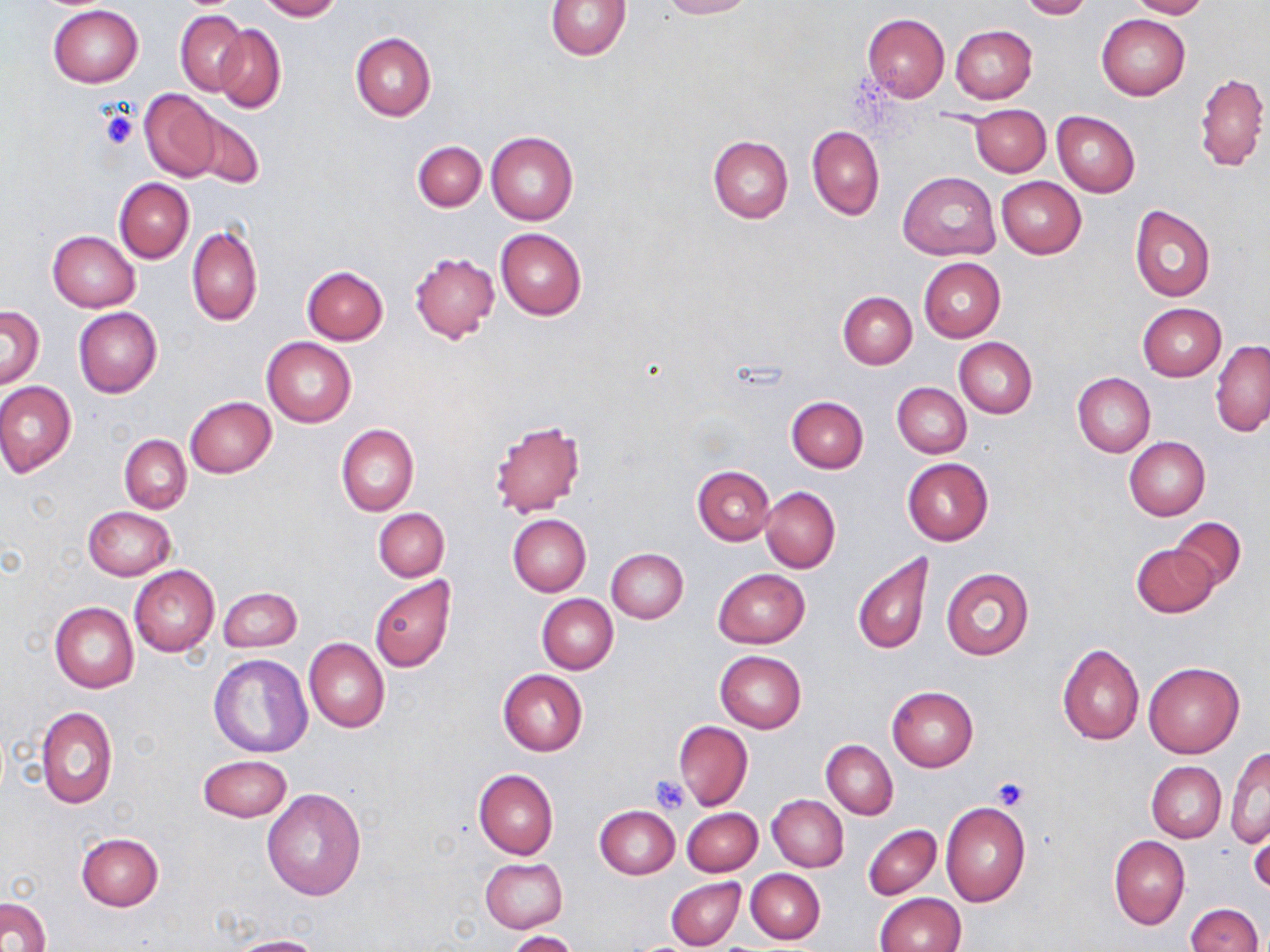

Approximate bounding boxes as named x1/y1/x2/y2 corners in pixels. Uninfected red blood cell locations: (x1=257, y1=0, x2=342, y2=21), (x1=546, y1=0, x2=632, y2=60), (x1=657, y1=0, x2=753, y2=19), (x1=1018, y1=0, x2=1092, y2=20), (x1=1126, y1=0, x2=1209, y2=18), (x1=49, y1=5, x2=142, y2=86), (x1=176, y1=11, x2=248, y2=95), (x1=861, y1=14, x2=950, y2=102), (x1=1097, y1=14, x2=1190, y2=100), (x1=214, y1=24, x2=286, y2=112), (x1=950, y1=25, x2=1037, y2=103), (x1=351, y1=31, x2=435, y2=120), (x1=1193, y1=72, x2=1268, y2=172), (x1=139, y1=89, x2=223, y2=181), (x1=971, y1=105, x2=1050, y2=175), (x1=1052, y1=111, x2=1140, y2=197), (x1=188, y1=112, x2=263, y2=190), (x1=808, y1=125, x2=884, y2=220), (x1=486, y1=131, x2=579, y2=225), (x1=708, y1=136, x2=793, y2=222), (x1=413, y1=140, x2=485, y2=212), (x1=898, y1=171, x2=998, y2=261), (x1=996, y1=176, x2=1087, y2=258), (x1=114, y1=178, x2=194, y2=262), (x1=1129, y1=205, x2=1216, y2=304), (x1=187, y1=225, x2=262, y2=326), (x1=496, y1=229, x2=587, y2=320), (x1=48, y1=230, x2=139, y2=311), (x1=409, y1=251, x2=499, y2=343), (x1=918, y1=258, x2=1005, y2=342), (x1=302, y1=267, x2=388, y2=345), (x1=838, y1=291, x2=917, y2=369), (x1=1137, y1=303, x2=1226, y2=381), (x1=0, y1=305, x2=44, y2=388), (x1=74, y1=306, x2=162, y2=399), (x1=261, y1=338, x2=356, y2=428), (x1=954, y1=338, x2=1037, y2=418), (x1=1210, y1=340, x2=1270, y2=437), (x1=1073, y1=372, x2=1154, y2=458), (x1=0, y1=381, x2=76, y2=478), (x1=892, y1=381, x2=971, y2=457), (x1=184, y1=396, x2=276, y2=478), (x1=787, y1=397, x2=868, y2=472), (x1=488, y1=420, x2=585, y2=519), (x1=336, y1=425, x2=417, y2=516), (x1=119, y1=434, x2=191, y2=513), (x1=1124, y1=437, x2=1210, y2=521), (x1=902, y1=458, x2=994, y2=546), (x1=693, y1=466, x2=774, y2=544), (x1=760, y1=486, x2=840, y2=573), (x1=85, y1=506, x2=175, y2=580), (x1=374, y1=508, x2=449, y2=581), (x1=508, y1=514, x2=591, y2=596), (x1=1171, y1=517, x2=1245, y2=590), (x1=1132, y1=543, x2=1218, y2=617), (x1=606, y1=547, x2=689, y2=623), (x1=852, y1=553, x2=933, y2=654), (x1=129, y1=565, x2=220, y2=657), (x1=940, y1=567, x2=1034, y2=661), (x1=713, y1=568, x2=809, y2=648), (x1=369, y1=577, x2=455, y2=673), (x1=218, y1=586, x2=301, y2=652), (x1=537, y1=594, x2=618, y2=674), (x1=49, y1=601, x2=139, y2=692), (x1=303, y1=638, x2=389, y2=733), (x1=1057, y1=643, x2=1145, y2=745), (x1=715, y1=651, x2=806, y2=732), (x1=208, y1=653, x2=314, y2=759), (x1=1143, y1=661, x2=1245, y2=759), (x1=498, y1=669, x2=587, y2=755), (x1=887, y1=686, x2=978, y2=771), (x1=36, y1=706, x2=117, y2=808), (x1=674, y1=720, x2=753, y2=810), (x1=823, y1=740, x2=897, y2=819), (x1=1226, y1=749, x2=1269, y2=849), (x1=198, y1=754, x2=292, y2=821), (x1=1146, y1=761, x2=1226, y2=843), (x1=474, y1=768, x2=558, y2=859), (x1=262, y1=787, x2=366, y2=900), (x1=767, y1=794, x2=848, y2=872), (x1=940, y1=801, x2=1032, y2=907), (x1=677, y1=805, x2=754, y2=946), (x1=595, y1=806, x2=679, y2=879), (x1=682, y1=808, x2=762, y2=876), (x1=1248, y1=820, x2=1269, y2=897), (x1=862, y1=824, x2=941, y2=900), (x1=76, y1=831, x2=163, y2=911), (x1=1109, y1=835, x2=1189, y2=930), (x1=480, y1=858, x2=568, y2=933), (x1=746, y1=869, x2=825, y2=944), (x1=666, y1=878, x2=743, y2=949), (x1=875, y1=892, x2=964, y2=952), (x1=2, y1=897, x2=51, y2=952), (x1=1186, y1=903, x2=1264, y2=952), (x1=507, y1=930, x2=579, y2=952), (x1=226, y1=935, x2=326, y2=952). Platelet locations: (x1=100, y1=108, x2=138, y2=149), (x1=649, y1=774, x2=690, y2=813), (x1=993, y1=777, x2=1029, y2=810). Slide-level diagnosis: no evidence of blood parasites. Captured at 1000x magnification. Image is 1270×952 pixels. Single field of view. Optical microscopy. May-Grünwald-Giemsa-stained preparation. Thin blood film.